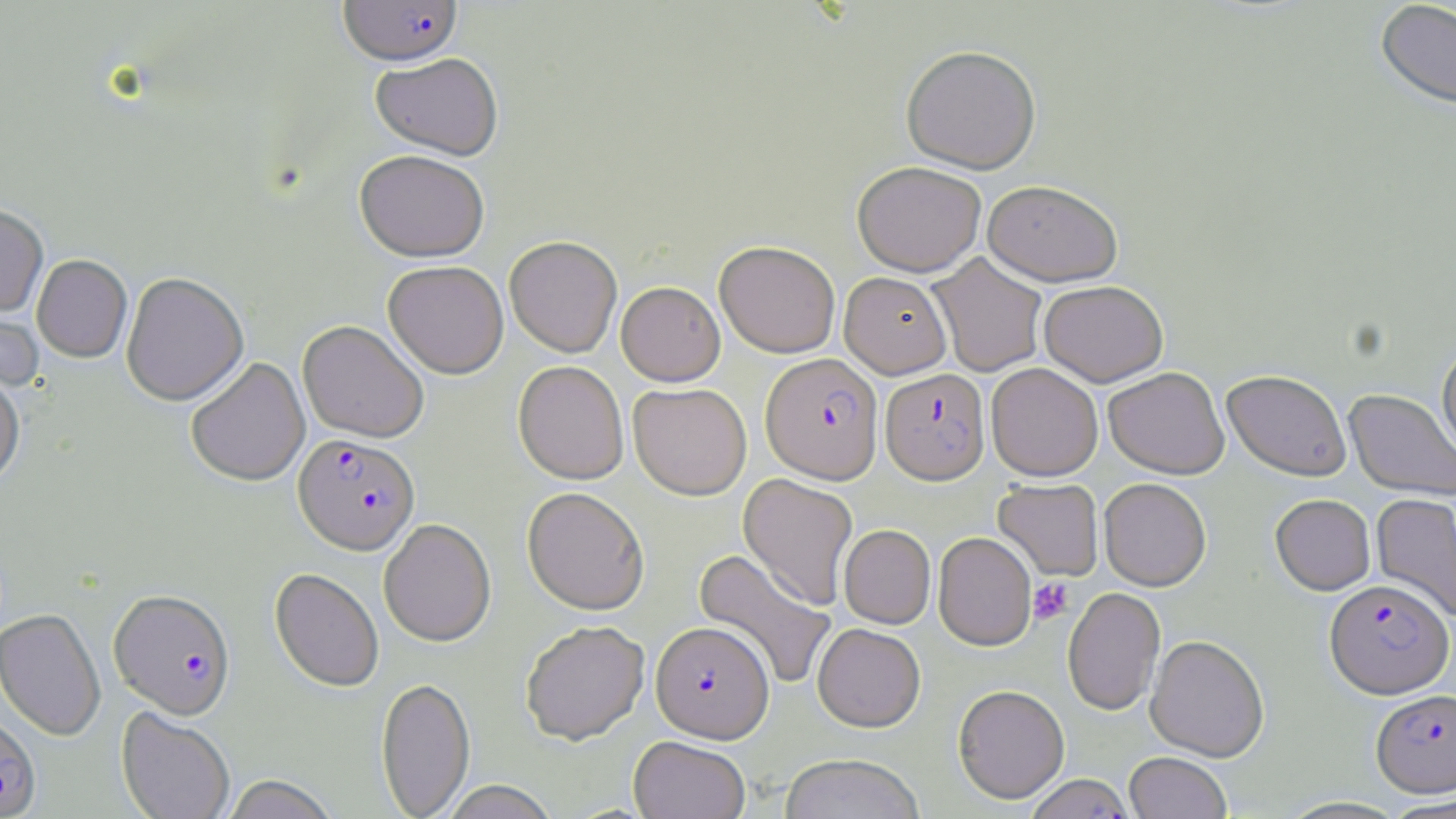
slide-level diagnosis = Plasmodium falciparum
platelet locations = approximate bounding boxes as (x1, y1, x2, y2) in pixels: (1028, 577, 1073, 624)
image size = 1456×819 pixels
uninfected red blood cell locations (subset) = approximate bounding boxes as (x1, y1, x2, y2) in pixels: (1375, 1, 1456, 111), (901, 44, 1041, 174), (371, 53, 503, 160), (354, 150, 490, 262), (852, 161, 986, 276), (982, 180, 1123, 286), (0, 204, 48, 316), (504, 236, 622, 357), (714, 240, 840, 357), (927, 252, 1048, 377), (32, 255, 132, 362), (383, 260, 509, 378), (839, 271, 952, 378), (121, 272, 248, 406), (1038, 280, 1169, 386), (616, 281, 725, 385), (0, 297, 45, 394), (297, 319, 429, 443), (1437, 341, 1456, 466), (186, 357, 310, 487), (513, 360, 629, 484), (986, 362, 1103, 481), (1103, 367, 1229, 479), (1222, 369, 1352, 481), (0, 370, 25, 489), (628, 382, 751, 500), (1344, 389, 1456, 502), (738, 473, 858, 610), (1099, 477, 1211, 591), (993, 478, 1104, 581), (522, 486, 650, 615), (1371, 492, 1456, 622), (1270, 493, 1376, 595), (379, 518, 496, 646), (839, 524, 935, 629), (933, 531, 1036, 650), (693, 548, 836, 689), (270, 568, 384, 692), (1063, 586, 1165, 715), (0, 608, 106, 741), (520, 620, 650, 745), (812, 623, 926, 732), (1145, 634, 1270, 761), (375, 677, 476, 818), (953, 684, 1070, 804), (116, 708, 235, 819), (628, 736, 750, 819), (1124, 752, 1232, 819), (780, 754, 925, 819), (221, 775, 340, 819), (438, 781, 560, 818), (1383, 795, 1456, 819)
stain = May-Grünwald-Giemsa
modality = light microscopy
Plasmodium falciparum-infected red blood cell locations (subset) = approximate bounding boxes as (x1, y1, x2, y2) in pixels: (338, 1, 463, 67), (761, 353, 884, 483), (880, 368, 990, 485), (293, 433, 420, 554), (1325, 578, 1453, 698), (109, 589, 235, 719), (651, 620, 773, 743), (1371, 688, 1456, 797), (0, 716, 41, 818)
preparation = thin blood smear
magnification = 1000x
field of view = one of a larger specimen